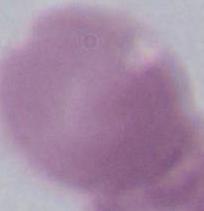

modality = micrograph
magnification = 1000x
identification = erythrocyte